Report the malaria status of this cell.
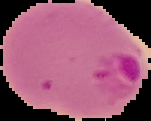
It is parasitized.

Segmented cell region on a black background. Image is 151×121 pixels. From a thin blood film.